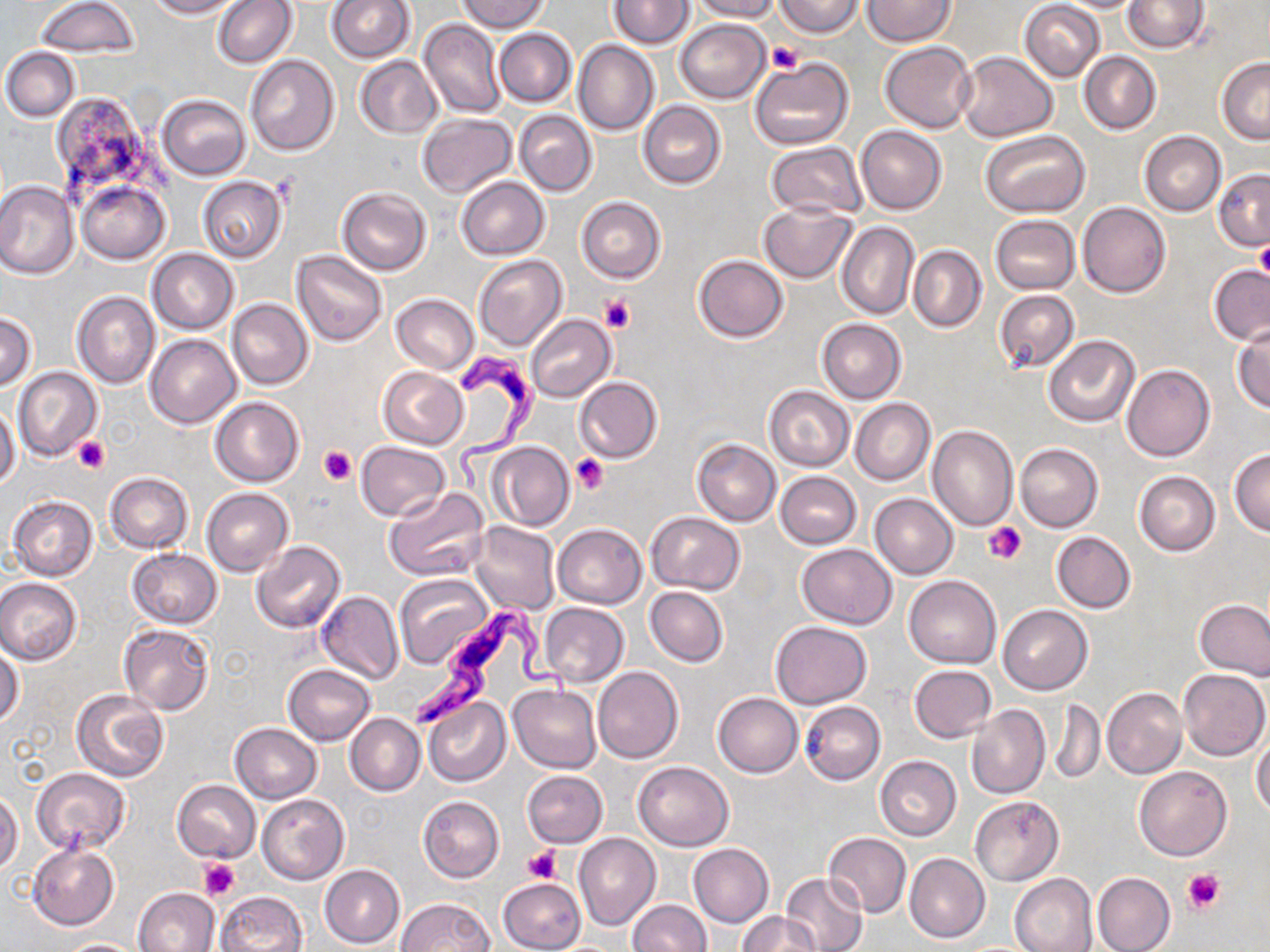
slide-level diagnosis = Trypanosoma brucei
platelet locations = approximate bounding boxes as (x1,y1)-(x2,y2) corner pairs in pixels: (769,41)-(803,74), (1254,242)-(1270,283), (599,294)-(636,334), (74,436)-(109,474), (319,446)-(357,485), (572,453)-(608,494), (982,521)-(1027,565), (524,848)-(562,885), (197,859)-(239,898), (1183,869)-(1224,912)
uninfected red blood cell locations = approximate bounding boxes as (x1,y1)-(x2,y2) corner pairs in pixels: (35,0)-(138,56), (145,0)-(244,18), (326,0)-(414,63), (458,0)-(548,32), (609,0)-(694,49), (689,0)-(780,22), (777,0)-(862,37), (862,0)-(953,47), (1053,0)-(1146,13), (1122,0)-(1210,53), (214,1)-(296,68), (1020,1)-(1106,81), (419,18)-(507,118), (674,18)-(770,103), (494,28)-(576,106), (574,41)-(659,135), (880,42)-(976,133), (2,47)-(80,121), (956,51)-(1057,142), (1078,51)-(1161,135), (245,55)-(339,155), (355,56)-(441,137), (1217,56)-(1270,143), (751,57)-(852,152), (156,95)-(249,180), (58,97)-(162,226), (639,100)-(726,188), (514,109)-(597,196), (416,113)-(516,198), (855,124)-(947,215), (1139,130)-(1226,215), (983,131)-(1089,217), (766,141)-(866,220), (1213,170)-(1270,251), (197,176)-(287,263), (456,176)-(549,260), (76,179)-(170,264), (0,181)-(77,280), (338,187)-(431,276), (577,196)-(665,282), (757,201)-(858,283), (1076,202)-(1170,297), (991,215)-(1080,293), (837,222)-(920,320), (909,246)-(986,332), (148,248)-(239,333), (292,250)-(387,346), (693,255)-(788,342), (473,256)-(566,351), (1209,264)-(1270,346), (993,289)-(1079,374), (72,291)-(160,389), (391,293)-(479,373), (227,298)-(313,390), (0,312)-(37,389), (525,313)-(616,402), (818,319)-(906,404), (1232,326)-(1270,414), (146,334)-(241,428), (1044,336)-(1139,426), (1122,364)-(1215,462), (378,367)-(468,449), (13,368)-(102,462), (573,376)-(663,462), (765,385)-(853,470), (211,396)-(305,486), (850,398)-(935,485), (0,403)-(20,490), (927,425)-(1019,532), (692,438)-(781,525), (356,441)-(451,521), (486,441)-(575,531), (1015,443)-(1103,531), (1229,447)-(1270,536), (1134,470)-(1220,556), (775,471)-(862,548), (104,472)-(194,552), (384,487)-(489,581), (203,488)-(293,576), (870,493)-(958,579), (9,495)-(99,580), (645,512)-(745,594), (469,521)-(560,615), (552,524)-(647,609), (1052,531)-(1136,612), (250,541)-(345,633), (797,543)-(896,628), (128,548)-(222,628), (394,574)-(493,670), (904,575)-(1001,667), (0,578)-(82,665), (645,587)-(728,667), (316,591)-(404,685), (1195,601)-(1270,678), (539,602)-(628,687), (997,604)-(1092,693), (770,620)-(871,707), (118,625)-(216,715), (0,645)-(25,729), (282,663)-(375,745), (909,664)-(997,743), (593,666)-(683,764), (1179,668)-(1269,760), (509,685)-(601,772), (1102,686)-(1186,779), (71,690)-(171,782), (713,692)-(803,778), (424,696)-(510,787), (1049,699)-(1105,784), (801,701)-(885,785), (965,704)-(1050,799), (346,713)-(425,796), (230,723)-(322,802), (1251,731)-(1270,818), (874,755)-(961,841), (632,761)-(735,850), (1134,766)-(1232,860), (31,767)-(129,853), (522,770)-(608,848), (172,779)-(260,862), (0,791)-(23,876), (257,794)-(349,884), (970,795)-(1063,885), (418,796)-(503,882), (574,833)-(659,931), (823,833)-(911,918), (27,843)-(119,929), (689,843)-(773,928), (904,852)-(990,943), (320,865)-(405,949), (779,872)-(867,952), (1092,872)-(1176,952), (1009,873)-(1098,952), (499,878)-(586,952), (134,888)-(218,952), (216,893)-(307,951), (395,897)-(493,952), (629,900)-(711,951), (737,910)-(822,952), (56,938)-(146,952)
stain = May-Grünwald-Giemsa
field of view = single
modality = optical microscopy
preparation = thin blood smear
Trypanosoma brucei locations = approximate bounding boxes as (x1,y1)-(x2,y2) corner pairs in pixels: (454,345)-(550,492), (409,598)-(575,731)
magnification = 1000x
image size = 1270×952 pixels